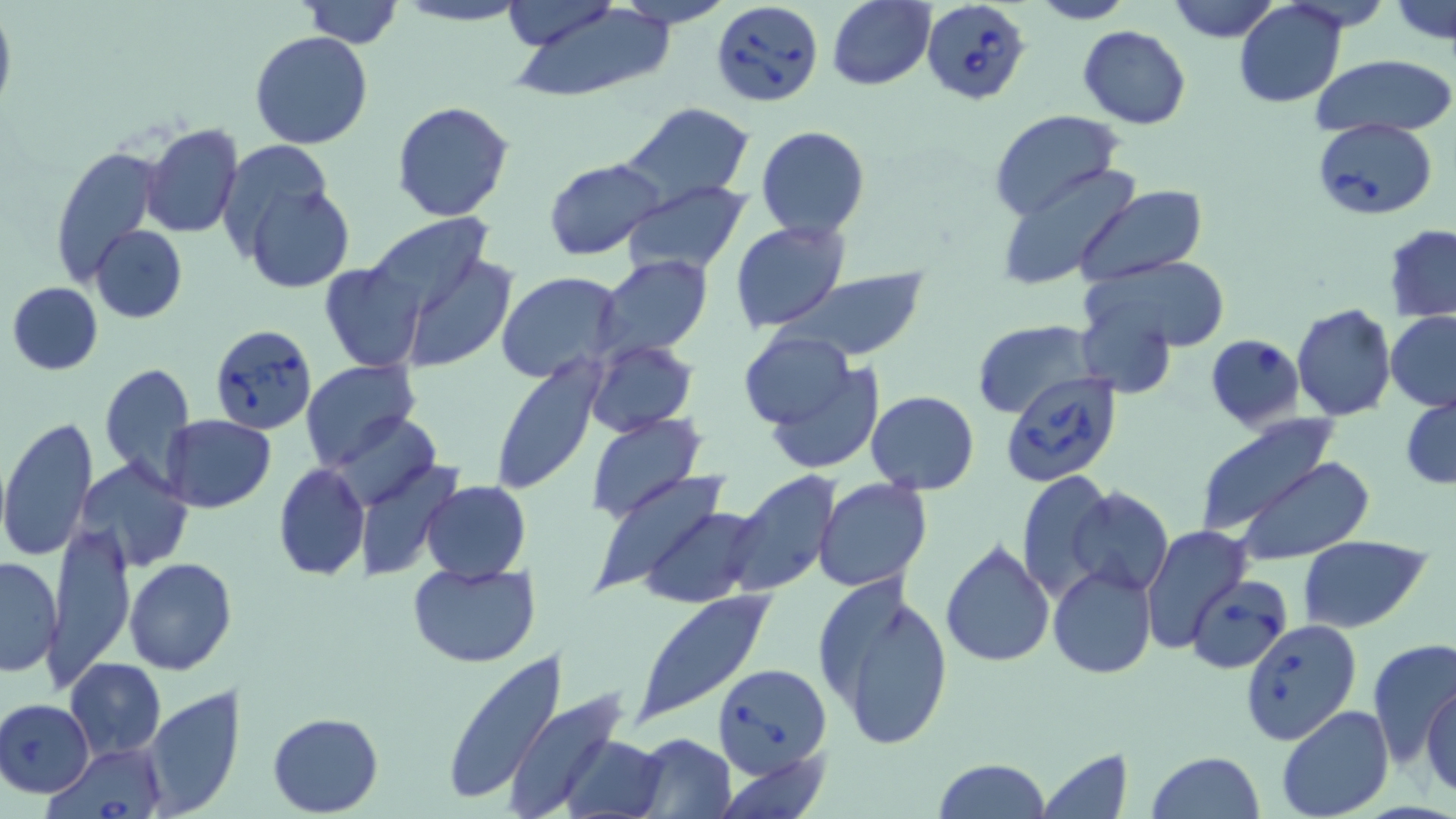

Summary:
  - Coordinate format: approximate bounding boxes as (x1, y1, x2, y2) in pixels
  - Uninfected red blood cell locations: (393, 0, 532, 27), (498, 0, 618, 48), (613, 0, 731, 28), (826, 0, 934, 90), (1027, 0, 1134, 25), (1165, 0, 1280, 43), (1391, 0, 1454, 48), (299, 1, 402, 49), (508, 2, 679, 102), (1235, 2, 1347, 108), (0, 10, 16, 116), (1078, 25, 1191, 129), (250, 30, 375, 149), (1308, 54, 1454, 138), (392, 100, 517, 222), (616, 103, 757, 208), (990, 110, 1123, 223), (141, 123, 243, 238), (756, 126, 870, 239), (222, 140, 338, 248), (50, 144, 163, 286), (545, 157, 664, 259), (993, 162, 1140, 289), (237, 175, 355, 294), (619, 183, 750, 278), (1073, 185, 1207, 289), (362, 215, 498, 326), (730, 220, 851, 333), (1385, 223, 1456, 321), (90, 225, 187, 322), (398, 249, 518, 372), (596, 256, 713, 360), (1085, 256, 1231, 355), (320, 262, 426, 372), (780, 268, 931, 361), (497, 273, 624, 386), (7, 282, 103, 375), (1078, 294, 1176, 398), (1291, 303, 1396, 420), (1385, 311, 1456, 411), (973, 321, 1097, 418), (738, 329, 857, 432), (585, 341, 698, 435), (486, 357, 606, 497), (301, 359, 421, 471), (100, 361, 197, 490), (764, 361, 886, 476), (866, 391, 980, 493), (1401, 394, 1456, 491), (329, 409, 441, 511), (586, 413, 707, 524), (161, 414, 276, 513), (0, 416, 98, 562), (1192, 416, 1344, 537), (1230, 457, 1376, 566), (75, 459, 193, 573), (273, 463, 370, 581), (357, 463, 461, 582), (590, 470, 740, 597), (726, 471, 843, 596), (1015, 471, 1115, 605), (812, 478, 933, 592), (421, 481, 530, 582), (1068, 487, 1174, 596), (635, 504, 765, 609), (45, 521, 135, 693), (1140, 524, 1251, 657), (1300, 537, 1430, 633), (938, 539, 1055, 667), (0, 555, 61, 677), (123, 558, 237, 675), (408, 561, 542, 669), (1048, 565, 1156, 678), (813, 573, 956, 751), (632, 590, 776, 724), (1239, 619, 1361, 746), (1367, 638, 1455, 770), (439, 650, 566, 804), (66, 657, 166, 760), (1422, 682, 1456, 800), (139, 686, 246, 816), (503, 692, 636, 819), (0, 699, 95, 797), (1276, 705, 1395, 819), (267, 713, 383, 816), (561, 731, 667, 819), (632, 733, 737, 818), (1037, 745, 1133, 818), (716, 748, 832, 819), (1145, 751, 1265, 819), (933, 758, 1052, 819)
  - Babesia divergens-infected red blood cell locations: (712, 0, 823, 104), (921, 1, 1031, 105), (1311, 118, 1438, 219), (210, 323, 317, 435), (1204, 334, 1306, 433), (1000, 369, 1123, 487), (1185, 575, 1293, 674), (715, 660, 831, 773), (52, 745, 165, 819)
  - Slide-level diagnosis: Babesia divergens
  - Stain: May-Grünwald-Giemsa
  - Field of view: one of a larger specimen
  - Magnification: 1000x
  - Modality: optical microscopy
  - Preparation: thin blood film
  - Image size: 1456×819 pixels